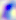

{
  "identification": "Toxoplasma gondii",
  "modality": "photomicrograph",
  "magnification": "400x"
}